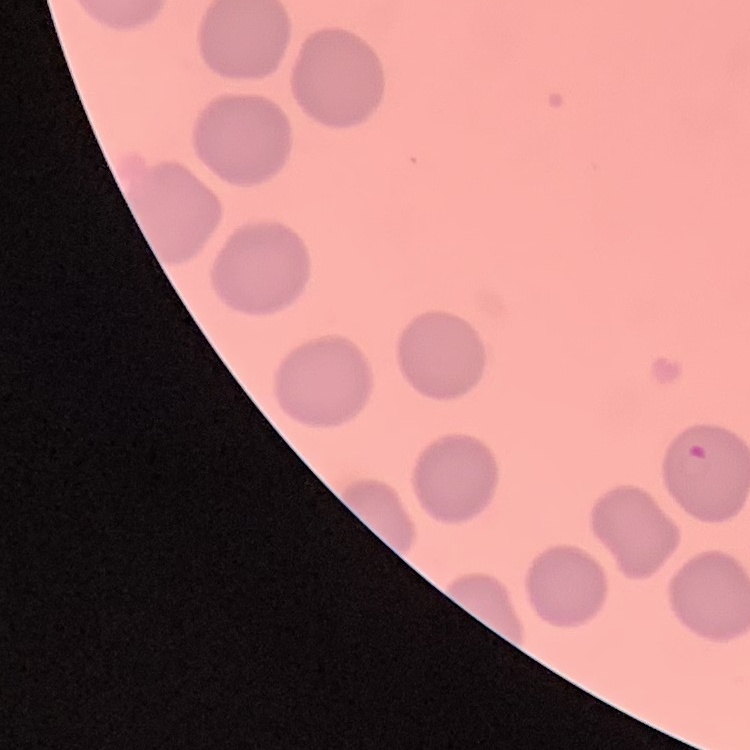
Summary:
  - Erythrocyte morphology: no rouleaux formation
  - Stain: Field's or Giemsa
  - Preparation: thin blood film
  - Image type: square crop of a larger photomicrograph